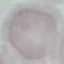

Summary:
  - Malaria status: uninfected
  - Preparation: thin blood smear
  - Stain: Giemsa
  - Capture: smartphone camera at the microscope eyepiece
  - Image type: cell patch, automatically extracted from a larger field of view and resized to 64 × 64 pixels